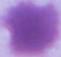
magnification = 1000x
identification = red blood cell
modality = photomicrograph